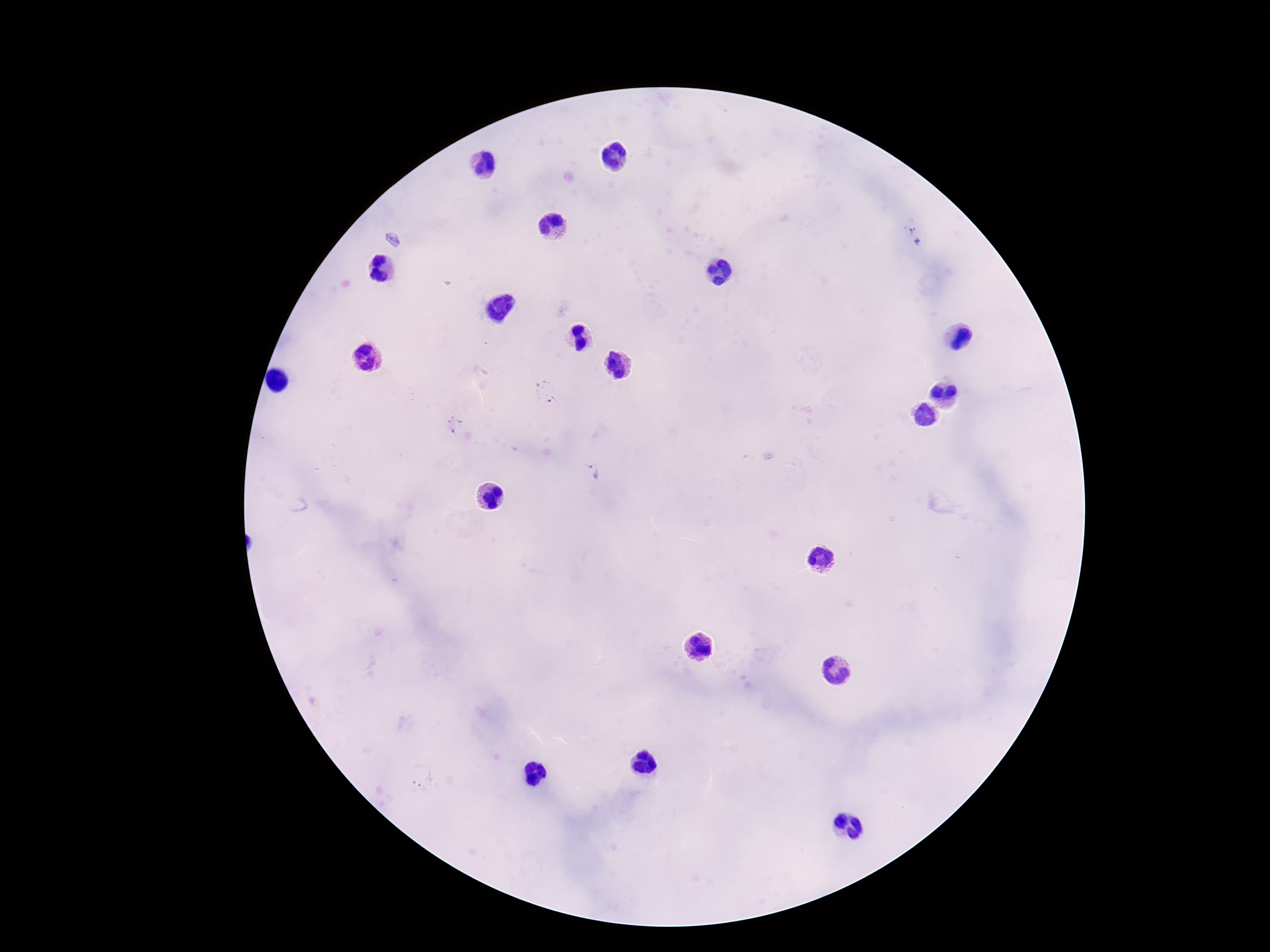
Approximate centers as [x, y] in pixels. Plasmodium parasite locations: [914, 237], [392, 240], [545, 391], [454, 424], [595, 473], [420, 777]. Photographed through the microscope eyepiece with a smartphone camera. 100x magnification. Giemsa-stained preparation. One field from this slide. Patient malaria status: positive. Thick blood film. Image is 1270×952 pixels.